Assess this cell for malaria.
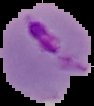
Parasitized.

Summary:
  - Preparation: thin blood smear
  - Image size: 94×106 pixels
  - Image type: segmented cell region on a black background